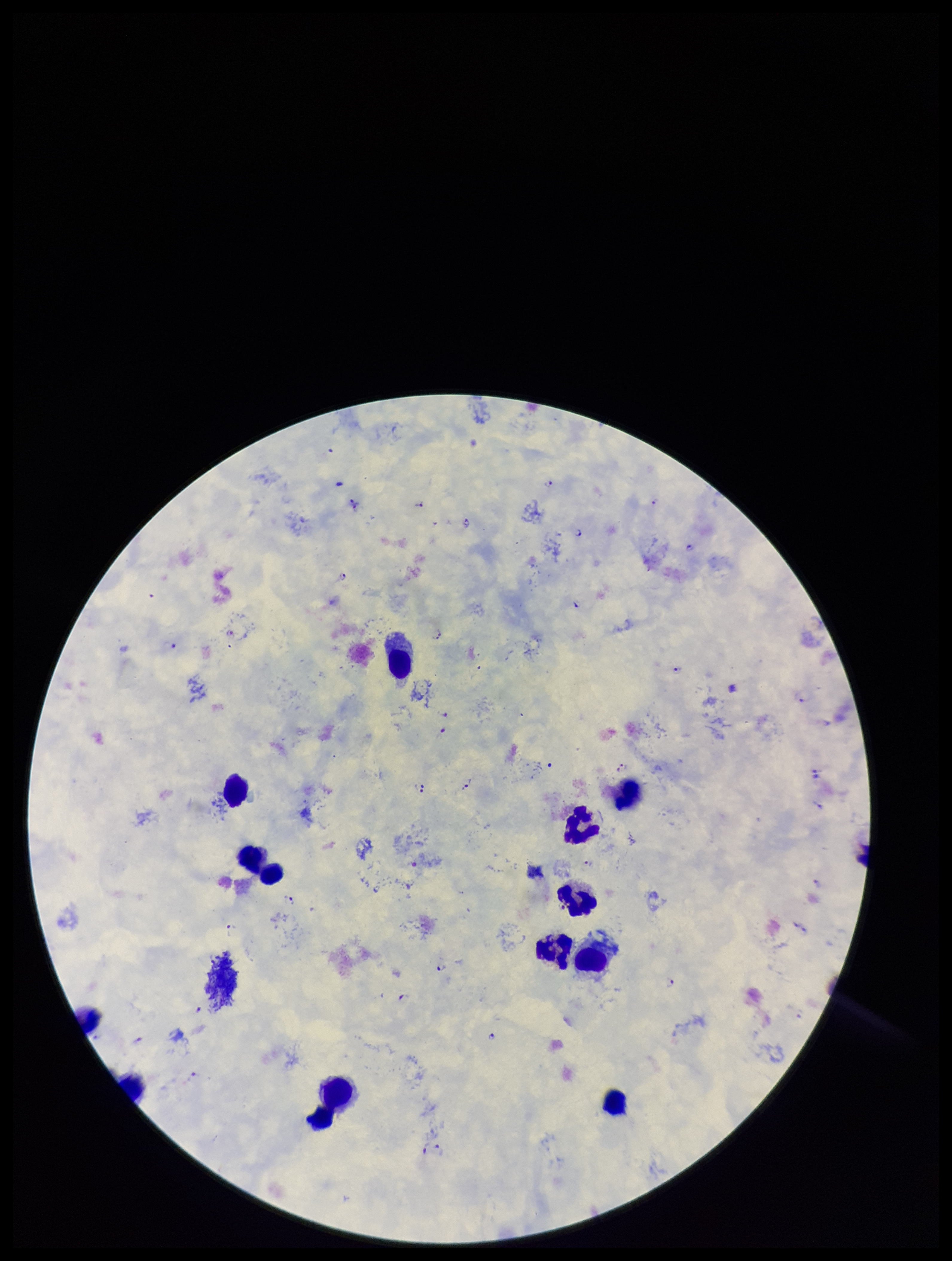

Summary:
  - Preparation: thick blood smear
  - Patient malaria status: infected
  - Image size: 952×1261 pixels
  - Plasmodium parasites: identified
  - Capture: smartphone photograph through the microscope eyepiece
  - Leukocyte count: 13
  - Parasite count: 28
  - Field of view: single
  - Stain: Giemsa
  - Species reported for this patient: Plasmodium falciparum